Name the parasite shown.
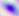

Toxoplasma gondii.

Summary:
  - Magnification: 400x
  - Modality: micrograph